Locate every uninfected red blood cell.
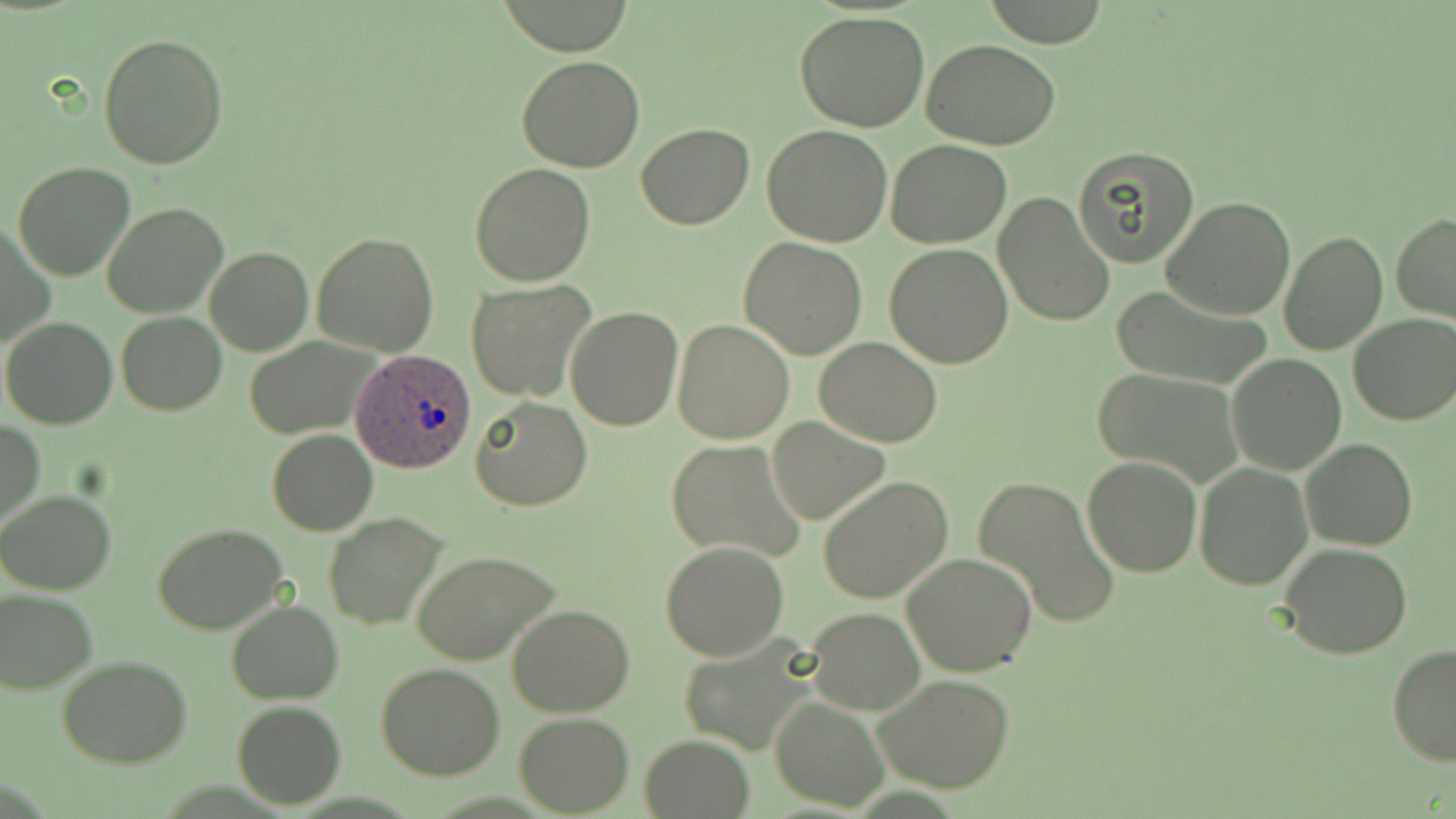
Approximate bounding boxes as (x1,y1)-(x2,y2) corner pairs in pixels.
Uninfected red blood cells: (981,0)-(1113,47), (795,12)-(931,132), (98,32)-(229,170), (922,38)-(1064,150), (515,56)-(645,173), (636,124)-(754,229), (762,124)-(892,247), (885,139)-(1012,249), (1072,145)-(1201,268), (12,162)-(136,282), (469,163)-(596,286), (993,190)-(1115,328), (1162,196)-(1296,320), (102,202)-(227,318), (1391,214)-(1456,323), (2,221)-(55,352), (1279,229)-(1389,356), (312,233)-(438,355), (739,237)-(868,359), (884,244)-(1015,369), (205,246)-(313,356), (466,281)-(596,401), (1108,284)-(1273,391), (566,306)-(683,430), (117,312)-(226,415), (1347,313)-(1456,425), (1,317)-(118,429), (672,318)-(796,443), (247,336)-(381,438), (814,338)-(943,447), (1227,354)-(1346,474), (1090,366)-(1245,485), (469,396)-(595,511), (767,417)-(891,524), (1,419)-(44,530), (266,429)-(378,535), (1301,436)-(1417,550), (667,439)-(806,562), (1081,455)-(1202,577), (1194,463)-(1311,589), (974,475)-(1120,628), (819,477)-(953,606), (0,491)-(118,596), (323,511)-(447,630), (153,523)-(292,634), (659,542)-(789,662), (1280,543)-(1415,659), (410,548)-(559,665), (902,553)-(1037,677), (0,588)-(97,695), (227,601)-(344,704), (508,604)-(635,716), (805,608)-(925,714), (675,628)-(826,754), (1388,644)-(1456,766), (57,655)-(192,768), (375,664)-(505,781), (870,673)-(1018,792), (771,694)-(889,810), (231,700)-(345,808), (514,712)-(634,816), (639,735)-(757,818).

Plasmodium ovale-infected red blood cell locations: (353,351)-(473,473). Slide-level diagnosis: Plasmodium ovale. Single field of view. May-Grünwald-Giemsa stain. Optical microscopy. Captured at 1000x magnification. Image is 1456×819 pixels. Thin blood film.